Classify this cell by malaria status.
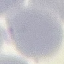
It is uninfected.

Thin blood smear. Giemsa stain. Automatically extracted cell patch, resized to 64 × 64 pixels. Photographed with a smartphone camera at the microscope eyepiece.